Identify the cell.
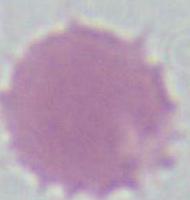

An erythrocyte.

1000x magnification. Micrograph.